Classify this cell by malaria status.
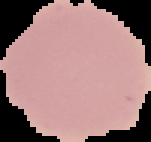
Uninfected.

From a thin blood film. Cell region segmented out of the field of view; the surrounding area is masked to black. Image is 151×142 pixels.